State the preparation type.
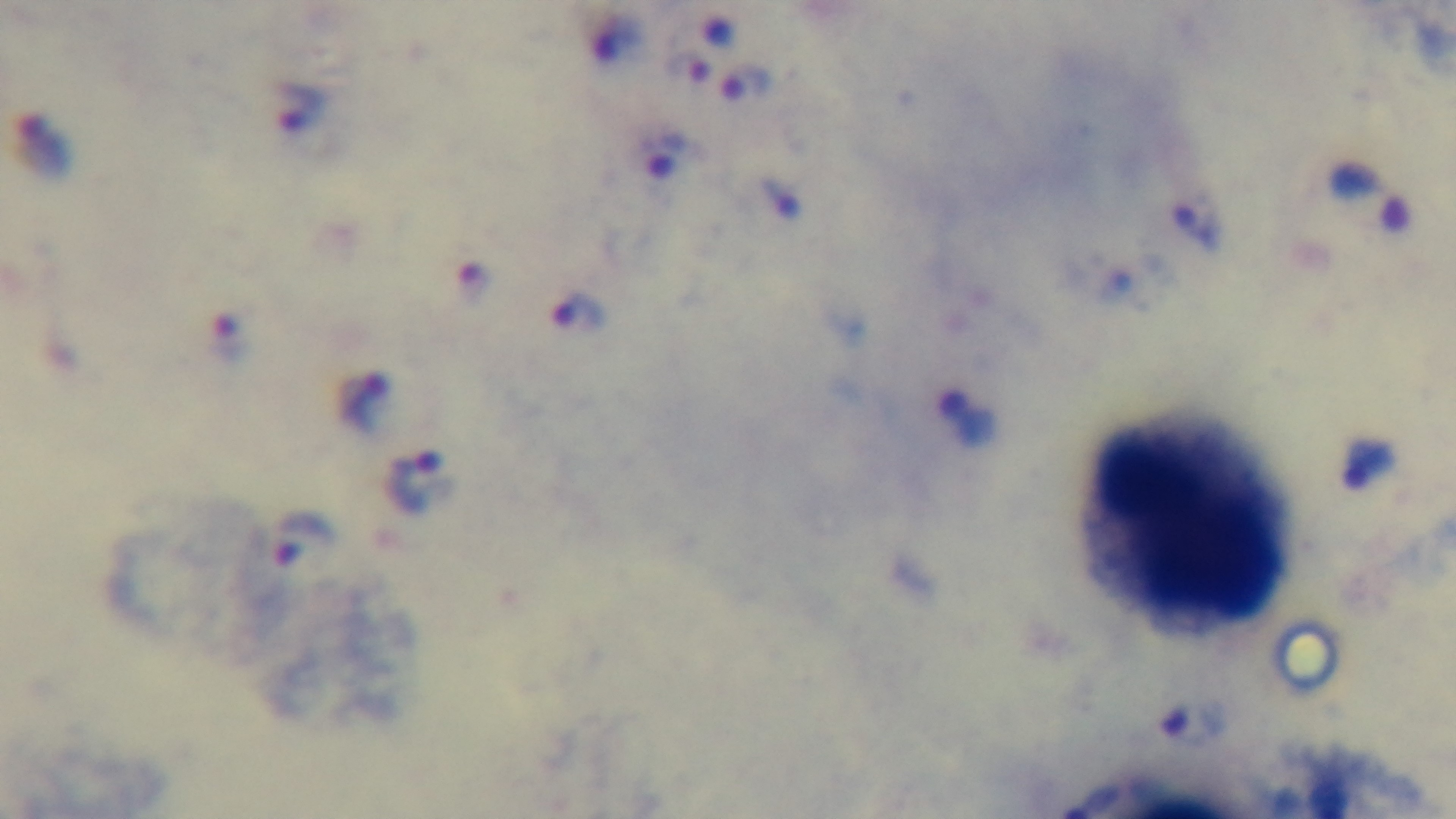

It is a thick blood film.

field of view = single
modality = light microscopy
malaria status = positive
stain = Giemsa
objective = 100x oil immersion
capture = mounted 4K digital camera